Classify this cell by malaria status.
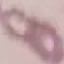

It is uninfected.

preparation = thin blood smear
capture = smartphone camera at the microscope eyepiece
image type = automatically extracted cell patch, resized to 64 × 64 pixels
stain = Giemsa